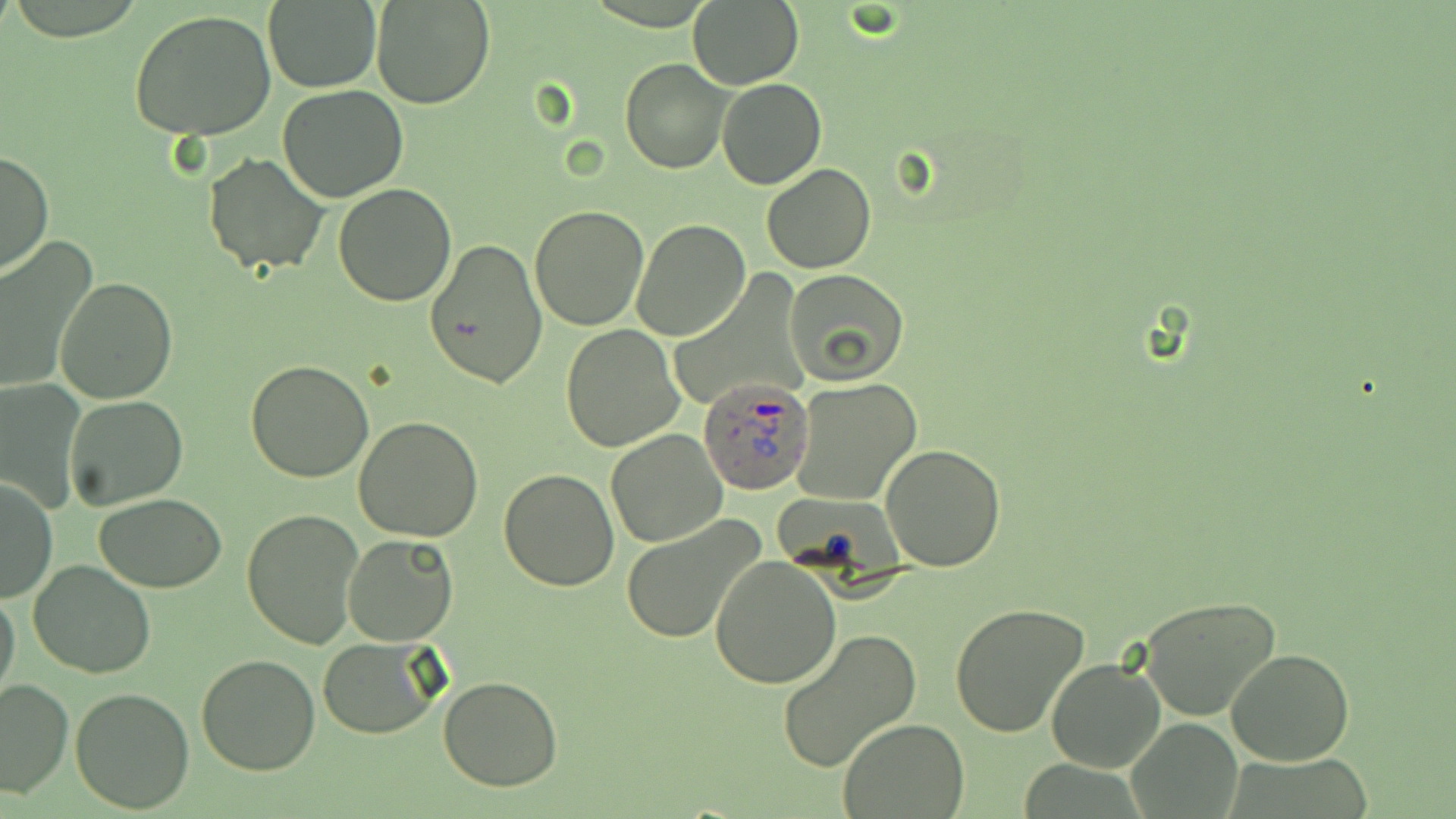

Approximate bounding boxes as (x1, y1, x2, y2) in pixels. Uninfected red blood cell locations: (370, 0, 493, 110), (263, 2, 381, 92), (687, 2, 804, 88), (129, 10, 277, 141), (620, 59, 731, 174), (716, 77, 826, 189), (279, 85, 407, 201), (0, 150, 53, 277), (203, 153, 329, 276), (762, 163, 876, 273), (334, 181, 456, 305), (530, 206, 650, 331), (630, 219, 751, 342), (0, 238, 93, 393), (424, 238, 548, 387), (784, 269, 908, 384), (55, 277, 178, 405), (560, 324, 685, 451), (246, 359, 375, 482), (791, 377, 923, 505), (1, 383, 86, 513), (64, 394, 187, 510), (353, 416, 485, 540), (606, 430, 726, 548), (879, 445, 1006, 571), (498, 468, 619, 591), (1, 477, 56, 604), (96, 494, 227, 592), (241, 508, 365, 649), (621, 517, 766, 644), (341, 534, 460, 647), (709, 555, 840, 687), (28, 559, 158, 678), (0, 584, 21, 708), (1137, 596, 1282, 720), (950, 602, 1089, 738), (775, 629, 922, 773), (319, 636, 444, 739), (1225, 647, 1354, 766), (195, 653, 322, 775), (1045, 657, 1165, 774), (438, 675, 564, 790), (0, 680, 71, 799), (70, 687, 196, 813), (1127, 719, 1241, 813), (836, 720, 970, 818). Plasmodium ovale-infected red blood cell locations: (699, 378, 816, 495). Slide-level diagnosis: Plasmodium ovale. 1000x magnification. May-Grünwald-Giemsa-stained preparation. Thin blood smear. Light microscopy. Image is 1456×819 pixels. One field of a larger specimen.